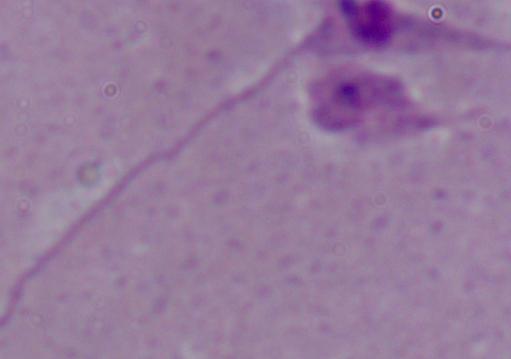
Summary:
  - Modality: photomicrograph
  - Magnification: 1000x
  - Identification: Leishmania